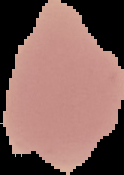
Segmented cell region on a black background. From a thin blood smear. Result: no Plasmodium parasites detected. Image is 124×175 pixels.